Outline each Plasmodium ovale-infected red blood cell.
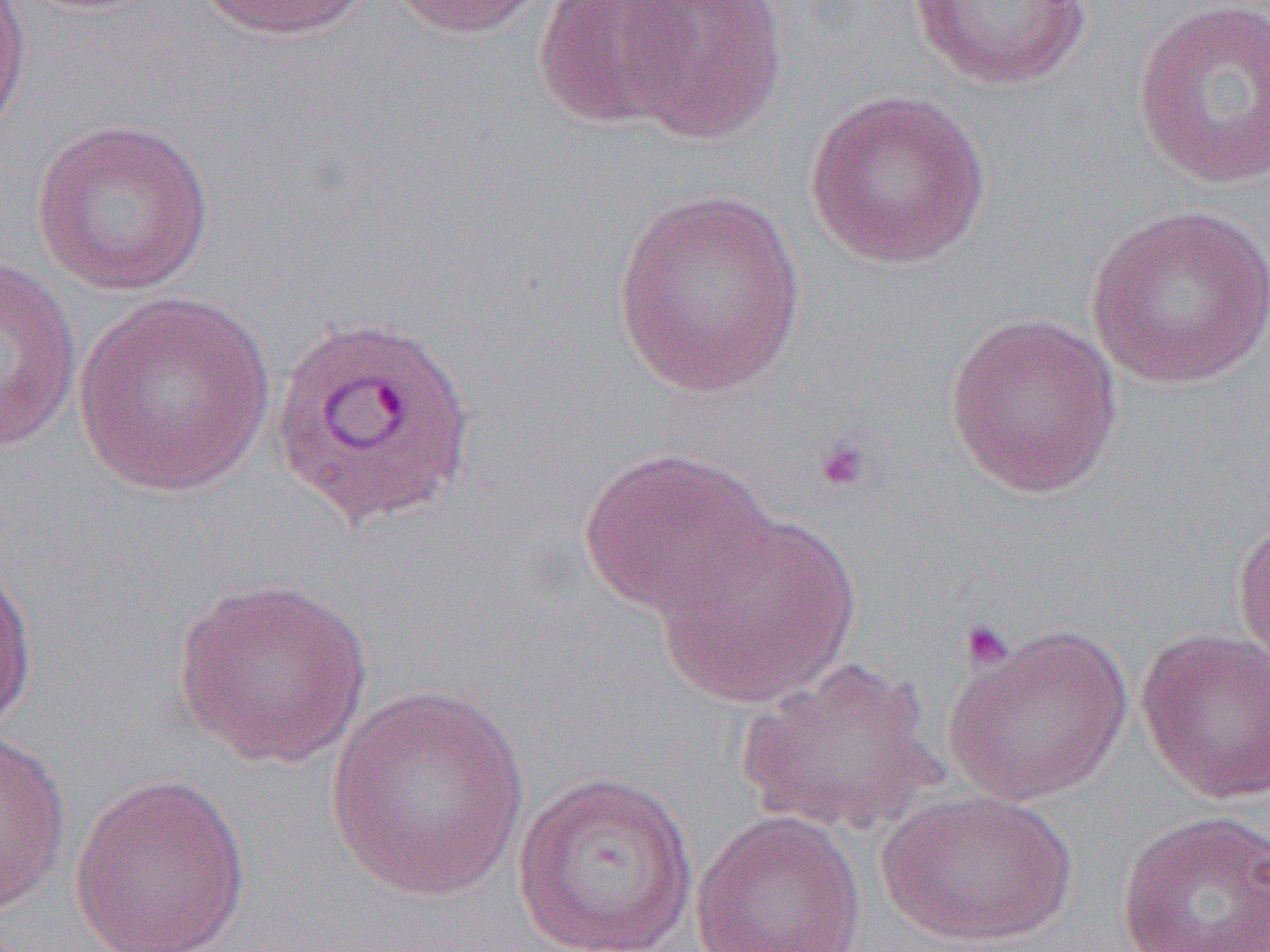
Approximate bounding boxes as (x1,y1)-(x2,y2) corner pairs in pixels.
Plasmodium ovale-infected red blood cells: (269,313)-(478,530).

slide-level diagnosis = Plasmodium ovale
preparation = thin blood smear
field of view = single
uninfected red blood cell locations = approximate bounding boxes as (x1,y1)-(x2,y2) corner pairs in pixels: (0,0)-(33,145), (195,0)-(373,41), (384,0)-(552,38), (534,0)-(697,130), (617,0)-(789,144), (907,0)-(1094,90), (1131,0)-(1269,190), (803,89)-(991,269), (30,117)-(216,296), (612,190)-(806,397), (1085,204)-(1270,389), (0,254)-(83,453), (73,291)-(277,497), (943,312)-(1123,498), (579,446)-(777,621), (653,512)-(862,708), (1231,515)-(1270,675), (0,555)-(39,737), (172,576)-(374,769), (942,623)-(1133,807), (1135,627)-(1270,804), (735,657)-(944,836), (326,685)-(531,900), (0,731)-(72,918), (511,771)-(700,952), (68,774)-(252,952), (876,786)-(1079,949), (690,808)-(866,952), (1116,809)-(1270,952)
platelet locations = approximate bounding boxes as (x1,y1)-(x2,y2) corner pairs in pixels: (813,437)-(872,494), (958,620)-(1016,672)
modality = optical microscopy
image size = 1270×952 pixels
magnification = 1000x